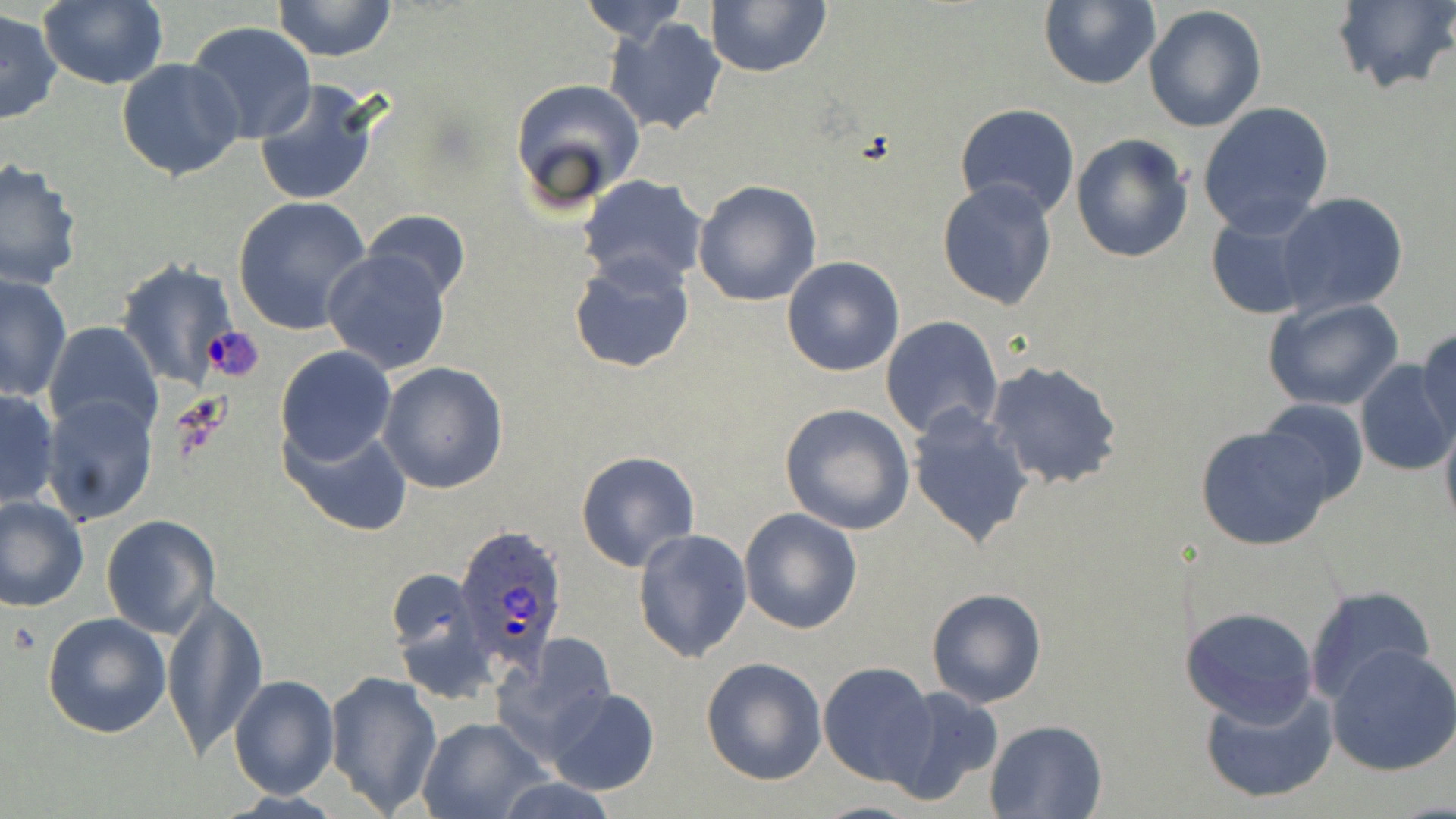
Approximate bounding boxes as (x1,y1)-(x2,y2) corner pairs in pixels. Plasmodium ovale-infected red blood cell locations: (453,523)-(571,673). Uninfected red blood cell locations: (38,0)-(167,90), (269,0)-(399,63), (574,0)-(692,45), (703,0)-(833,78), (1331,0)-(1455,96), (1038,1)-(1160,89), (1144,5)-(1267,133), (1,8)-(64,125), (604,19)-(728,138), (184,21)-(317,144), (116,56)-(246,181), (509,77)-(646,211), (253,80)-(383,208), (1196,102)-(1334,238), (954,104)-(1080,221), (1071,133)-(1194,262), (0,159)-(81,290), (576,175)-(709,291), (693,179)-(822,305), (937,179)-(1059,311), (1274,193)-(1409,317), (232,196)-(373,337), (360,209)-(470,306), (1205,210)-(1316,319), (322,249)-(453,377), (568,252)-(696,376), (782,257)-(904,375), (116,258)-(238,390), (2,271)-(72,400), (1263,297)-(1404,412), (880,316)-(1004,440), (43,323)-(163,442), (1416,328)-(1455,440), (275,345)-(397,466), (984,360)-(1123,491), (1354,361)-(1456,476), (378,362)-(509,494), (0,387)-(59,511), (38,392)-(162,526), (1257,397)-(1370,507), (780,404)-(915,534), (906,404)-(1036,548), (1439,412)-(1456,539), (283,423)-(413,536), (1196,424)-(1332,551), (576,450)-(701,573), (0,494)-(89,612), (738,508)-(862,634), (101,516)-(220,640), (631,527)-(754,665), (386,563)-(485,681), (1305,584)-(1435,705), (925,587)-(1046,708), (159,589)-(268,761), (1181,605)-(1319,724), (41,612)-(171,737), (503,633)-(615,749), (1327,644)-(1456,777), (700,656)-(828,786), (818,661)-(939,785), (326,671)-(442,816), (228,674)-(340,800), (1199,682)-(1339,805), (543,686)-(660,795), (883,686)-(1004,806), (417,717)-(550,819), (985,718)-(1109,817), (495,776)-(621,819). Slide-level diagnosis: Plasmodium ovale. Thin blood smear. Light microscopy. One field of a larger specimen. Image is 1456×819 pixels. 1000x magnification. May-Grünwald-Giemsa-stained preparation.